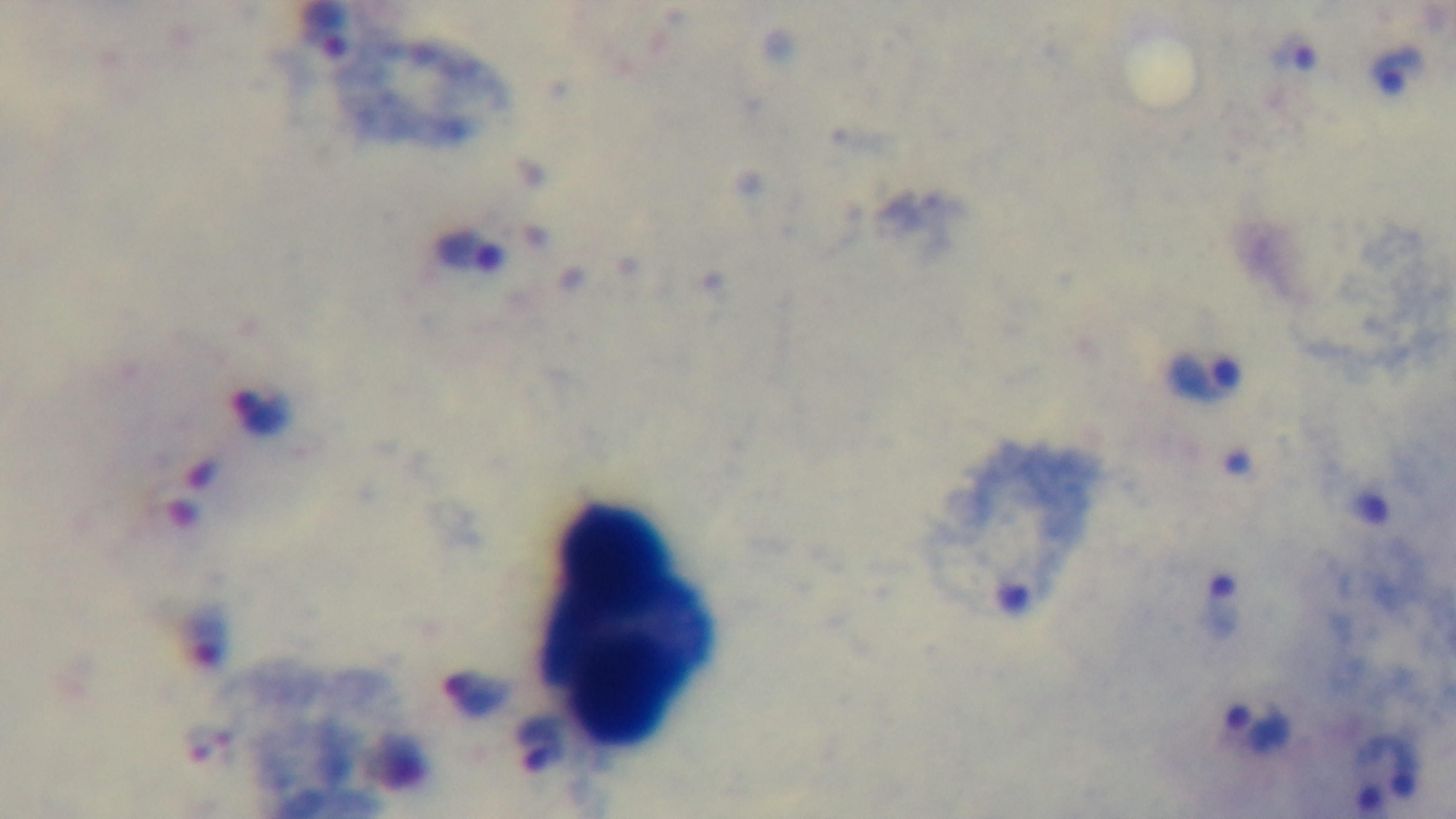

{
  "capture": "mounted 4K digital camera",
  "preparation": "thick blood film",
  "objective": "100x oil immersion",
  "stain": "Giemsa",
  "malaria_status": "positive",
  "modality": "light microscopy",
  "field_of_view": "single"
}